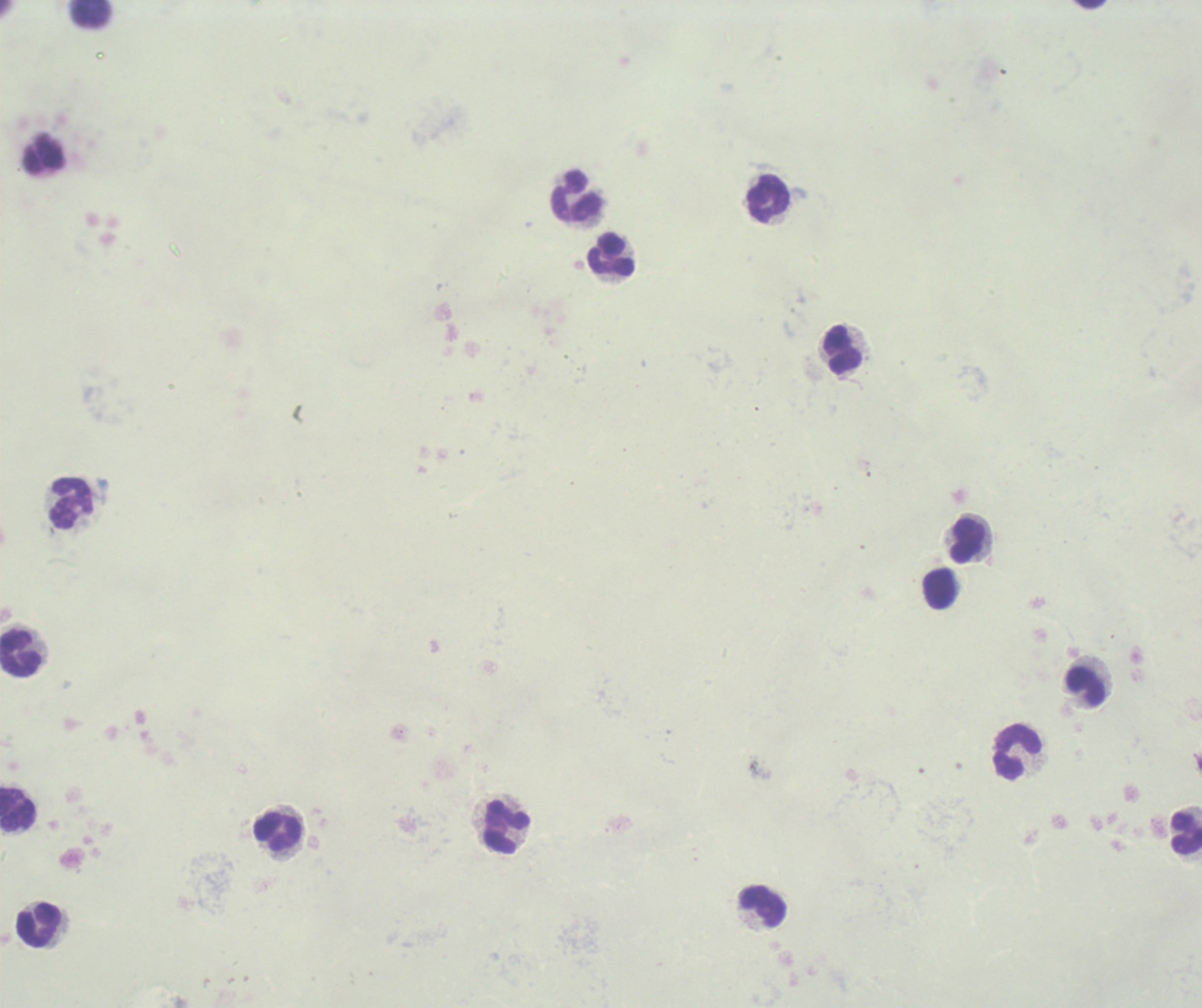
magnification: 100x
image_size: 1202×1008 pixels
stain: Romanowsky
context: previously used in an actual diagnosis
result: no malaria parasites detected
field_of_view: one from this slide
background_quality: poor
leukocyte_locations: 'approximate centers as {x, y} in pixels: {91, 14}, {43, 156}, {576, 198}, {768, 199}, {612, 255}, {841, 351}, {72, 504}, {967, 541}, {939, 588}, {21, 654}, {1085, 688}, {1019, 753}, {17, 812}, {506, 828}, {278, 832}, {1186, 833}, {762, 906}, {37, 927}'
preparation: thick smear of blood